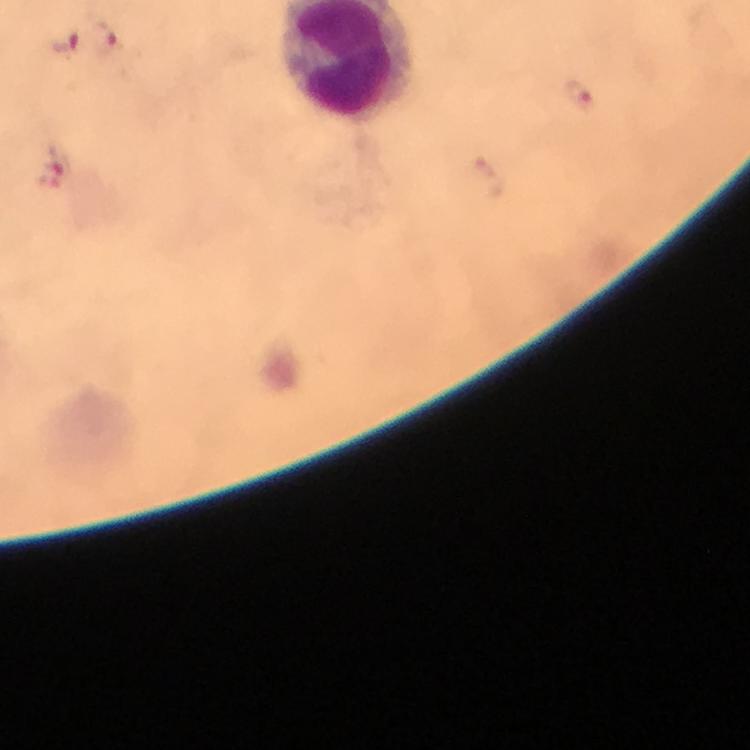
Approximate centers as {x, y} in pixels.
Summary:
  - Plasmodium parasite locations: {104, 41}, {63, 42}, {581, 96}, {56, 169}
  - Stain: Giemsa
  - Context: from a malaria diagnostic workup
  - Cropped from: a single field of view
  - Capture: smartphone photograph through a microscope
  - Preparation: thick blood film
  - Magnification: 100x
  - Immersion oil: applied
  - Image size: 750×750 pixels